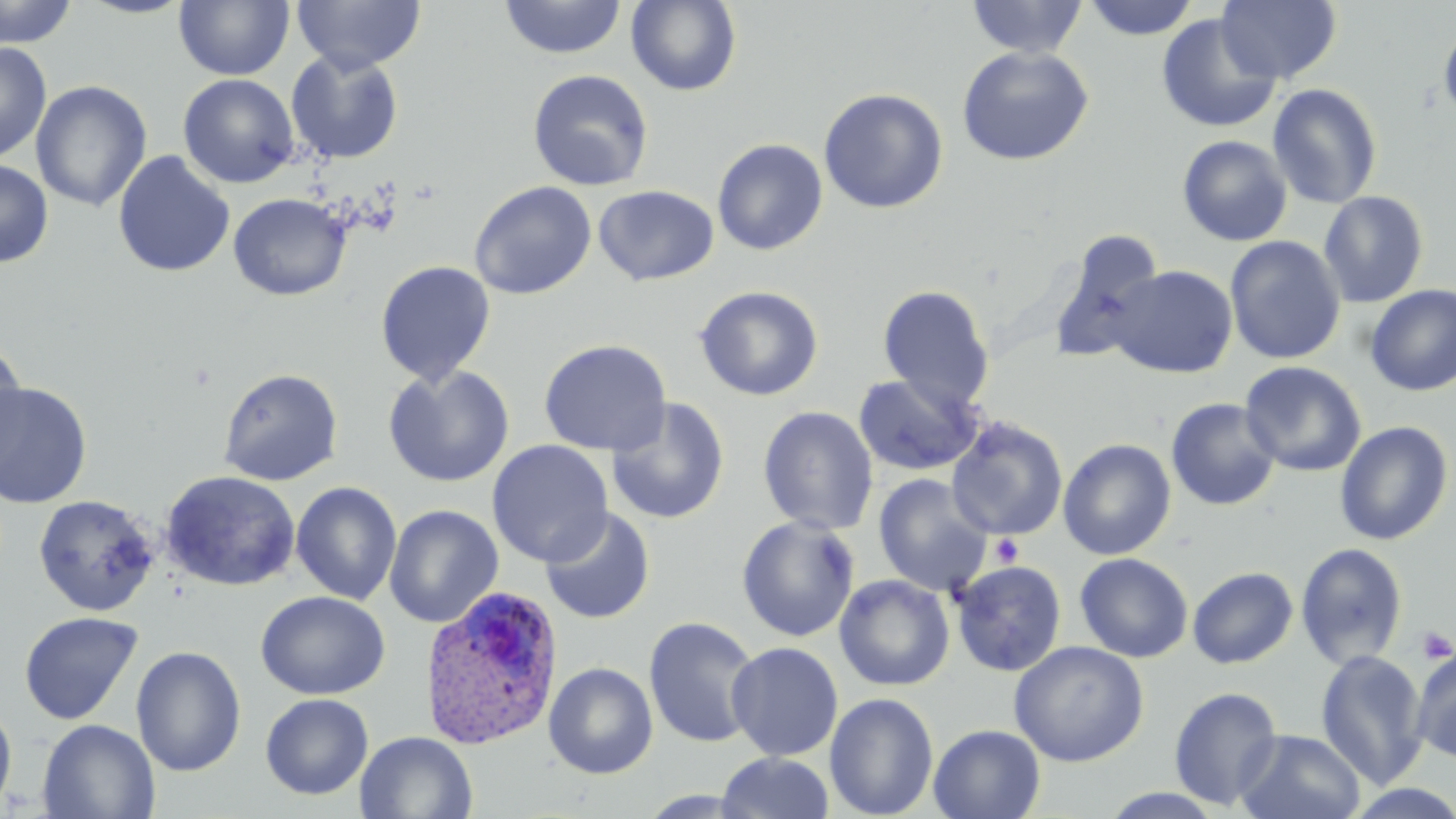

slide_level_diagnosis: Plasmodium ovale
image_size: 1456×819 pixels
plasmodium_ovale_infected_red_blood_cell_locations: 'approximate bounding boxes as [x1, y1, x2, y2] in pixels: [419, 584, 565, 749]'
platelet_locations: 'approximate bounding boxes as [x1, y1, x2, y2] in pixels: [991, 534, 1024, 567], [1415, 625, 1455, 665]'
magnification: 1000x
stain: May-Grünwald-Giemsa
preparation: thin blood film
modality: light microscopy
uninfected_red_blood_cell_locations: 'approximate bounding boxes as [x1, y1, x2, y2] in pixels: [0, 0, 78, 48], [77, 0, 196, 19], [173, 0, 294, 80], [499, 0, 626, 60], [966, 0, 1089, 59], [1082, 0, 1200, 40], [1216, 0, 1342, 84], [292, 1, 426, 74], [625, 1, 743, 96], [1155, 12, 1282, 134], [1438, 18, 1456, 128], [0, 41, 52, 163], [956, 45, 1094, 165], [286, 49, 405, 164], [527, 69, 655, 191], [178, 73, 300, 188], [30, 80, 152, 212], [1267, 83, 1383, 210], [818, 87, 948, 214], [1177, 135, 1293, 247], [712, 138, 828, 255], [113, 150, 235, 278], [0, 158, 53, 268], [469, 181, 597, 300], [593, 184, 719, 286], [1318, 190, 1429, 308], [228, 193, 351, 300], [1048, 231, 1166, 365], [1225, 235, 1346, 364], [375, 260, 497, 386], [1109, 265, 1238, 378], [1365, 284, 1456, 395], [694, 285, 824, 401], [877, 285, 995, 412], [538, 339, 672, 456], [0, 343, 29, 478], [1239, 361, 1367, 477], [382, 365, 515, 488], [218, 368, 343, 486], [853, 372, 983, 477], [0, 381, 93, 509], [606, 398, 730, 524], [1165, 398, 1282, 511], [757, 405, 879, 535], [946, 416, 1068, 541], [1334, 421, 1453, 546], [1058, 438, 1176, 560], [487, 440, 614, 567], [161, 470, 300, 591], [872, 474, 993, 596], [290, 481, 402, 605], [33, 494, 159, 617], [384, 504, 504, 629], [539, 507, 656, 624], [735, 514, 860, 642], [1295, 542, 1409, 670], [1074, 552, 1193, 662], [950, 560, 1067, 677], [1187, 566, 1298, 668], [834, 574, 955, 691], [255, 590, 391, 700], [18, 611, 144, 725], [643, 615, 762, 749], [1008, 640, 1149, 767], [726, 641, 843, 761], [131, 645, 247, 777], [1411, 647, 1456, 763], [1315, 649, 1430, 790], [544, 662, 658, 779], [1169, 686, 1283, 810], [259, 693, 373, 800], [825, 693, 939, 818], [0, 701, 17, 815], [38, 719, 160, 818], [928, 724, 1046, 819], [1235, 729, 1366, 818], [355, 732, 478, 819], [716, 751, 834, 819], [1097, 788, 1230, 819]'
field_of_view: one of a larger specimen